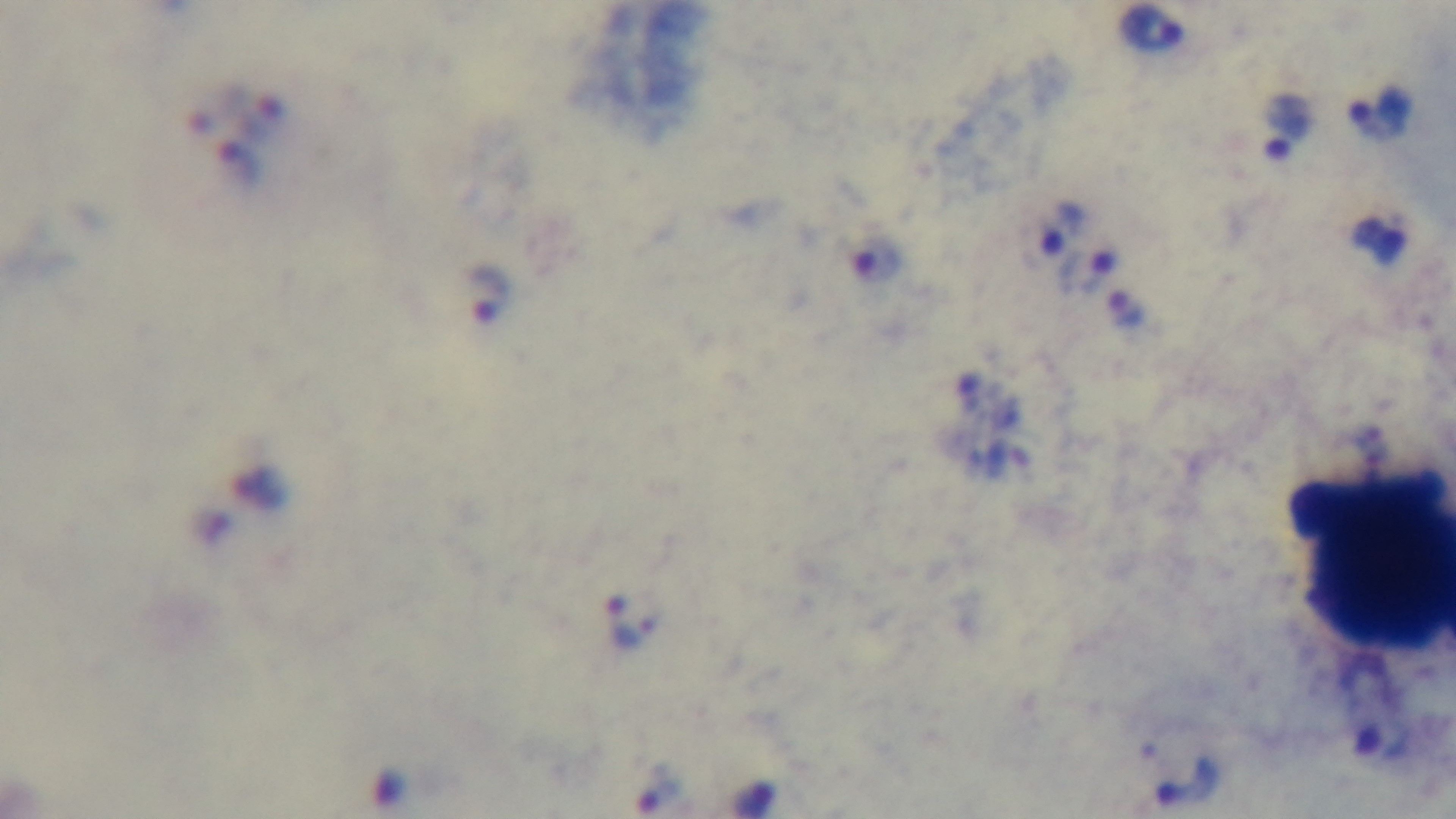
objective = 100x oil immersion
malaria status = infected
field of view = one from the slide
capture = mounted 4K digital camera
preparation = thick
stain = Giemsa
modality = light microscopy